Name the blood parasite species.
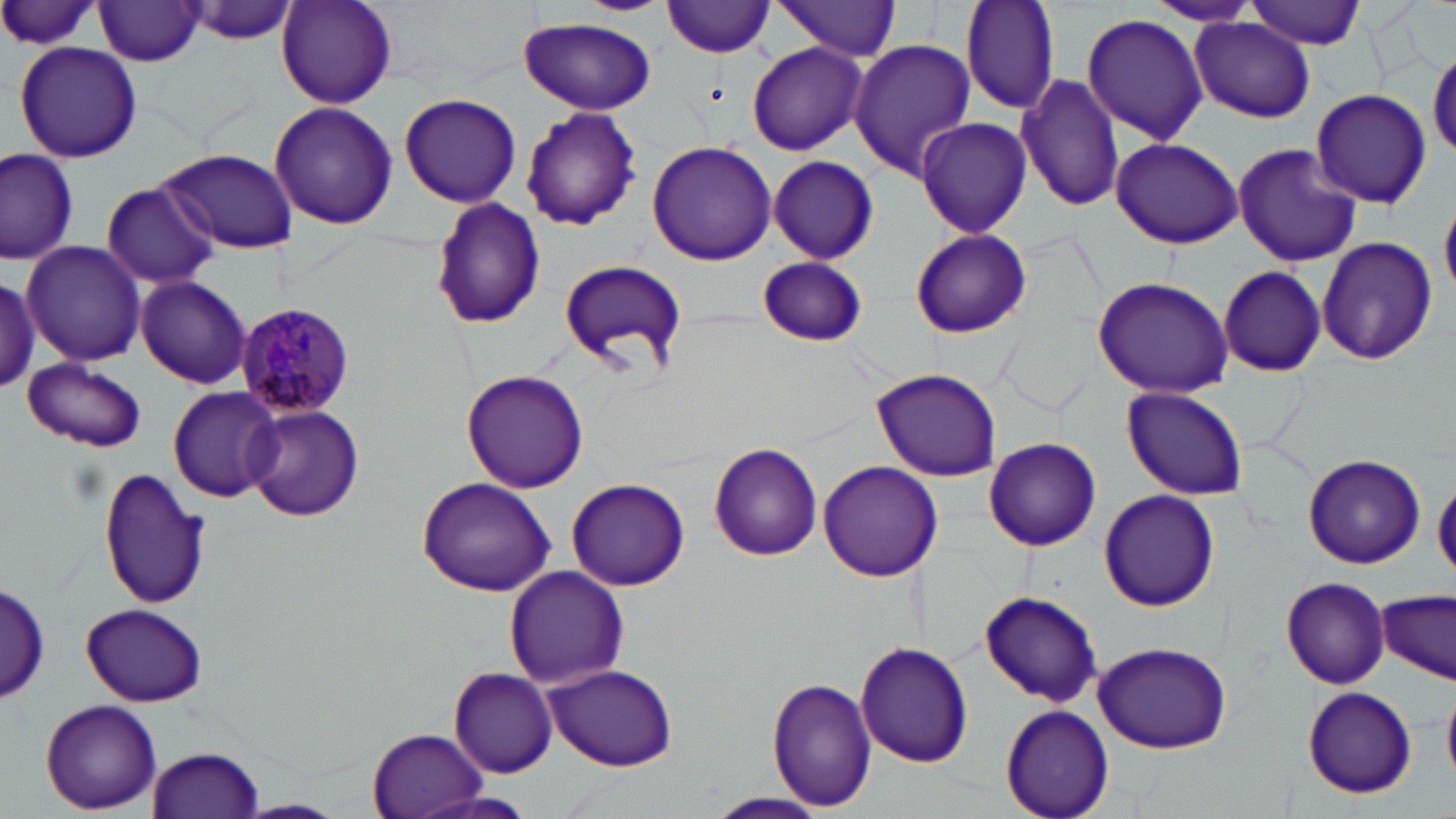
Plasmodium malariae.

Summary:
  - Coordinate format: approximate bounding boxes as (x1, y1, x2, y2) in pixels
  - Uninfected red blood cell locations: (0, 0, 105, 52), (179, 0, 305, 47), (276, 0, 400, 110), (572, 0, 675, 16), (959, 0, 1060, 115), (1143, 0, 1262, 27), (662, 1, 777, 57), (1244, 1, 1368, 49), (93, 2, 208, 66), (769, 2, 903, 60), (1082, 13, 1210, 143), (518, 16, 656, 115), (1190, 19, 1315, 122), (849, 41, 976, 180), (12, 42, 144, 165), (746, 42, 868, 157), (1429, 48, 1456, 158), (1016, 72, 1123, 212), (1310, 87, 1432, 209), (397, 94, 522, 208), (270, 102, 398, 230), (519, 105, 642, 230), (914, 117, 1031, 238), (1109, 138, 1244, 248), (647, 140, 777, 266), (1232, 140, 1362, 269), (0, 146, 78, 266), (157, 148, 298, 254), (768, 155, 878, 264), (99, 180, 220, 289), (1440, 195, 1455, 301), (429, 198, 547, 329), (910, 229, 1031, 338), (1316, 234, 1437, 366), (21, 241, 147, 365), (756, 256, 870, 347), (557, 258, 688, 377), (1219, 265, 1327, 378), (0, 272, 40, 397), (134, 276, 252, 388), (1090, 276, 1234, 397), (23, 359, 147, 452), (871, 367, 1002, 482), (461, 369, 589, 494), (167, 386, 282, 503), (1122, 388, 1248, 500), (244, 404, 365, 522), (984, 436, 1102, 551), (709, 444, 823, 561), (1303, 453, 1425, 569), (817, 461, 943, 581), (97, 466, 212, 611), (566, 476, 691, 591), (1433, 477, 1456, 581), (416, 478, 555, 597), (1098, 489, 1219, 611), (504, 566, 629, 688), (1282, 576, 1390, 688), (0, 579, 51, 704), (979, 589, 1104, 707), (1376, 591, 1455, 683), (80, 603, 206, 706), (854, 641, 974, 767), (1091, 641, 1231, 754), (542, 664, 678, 770), (448, 667, 557, 777), (767, 678, 878, 811), (1301, 686, 1418, 799), (1444, 688, 1456, 783), (40, 699, 161, 813), (1001, 705, 1113, 819), (367, 729, 485, 818), (148, 747, 265, 818), (704, 792, 830, 818)
  - Plasmodium malariae-infected red blood cell locations: (235, 302, 358, 418)
  - Modality: light microscopy
  - Image size: 1456×819 pixels
  - Stain: May-Grünwald-Giemsa
  - Preparation: thin blood smear
  - Magnification: 1000x
  - Field of view: single